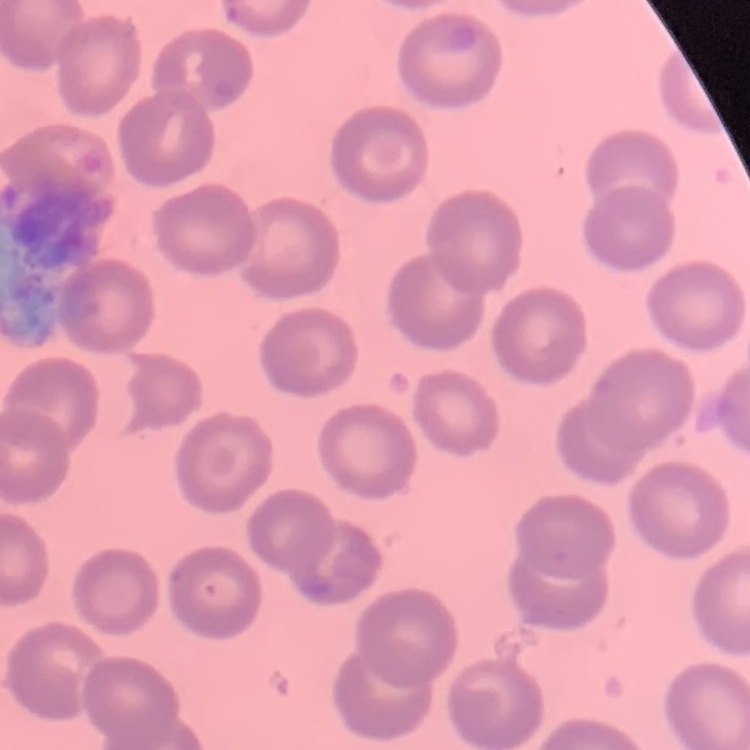

The erythrocytes show no rouleaux formation. One tile cut from a larger photomicrograph. Thin peripheral smear. Field's or Giemsa stain.